Assess the morphology of the red blood cells.
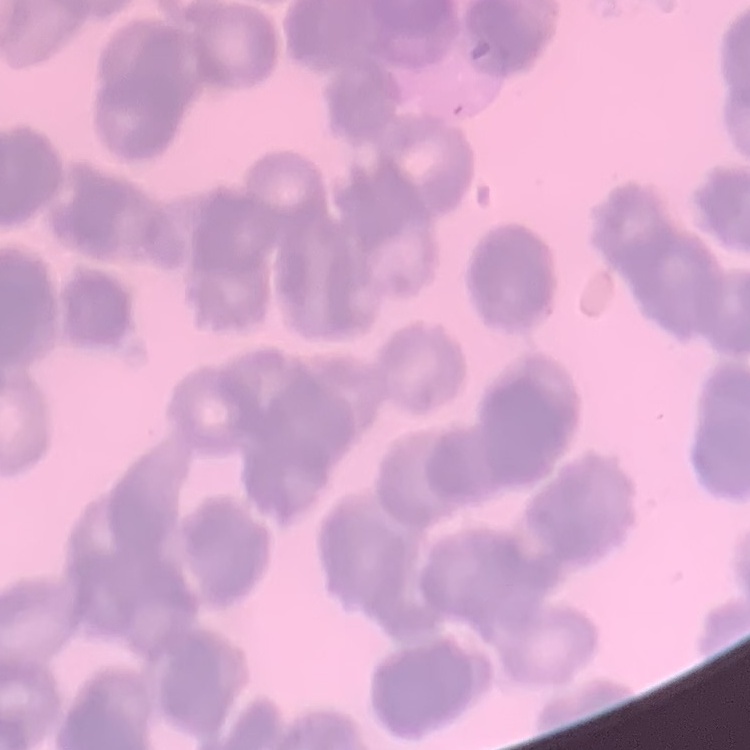
Rouleaux formation.

image type = square crop of a larger photomicrograph
preparation = thin blood smear
stain = Field's or Giemsa